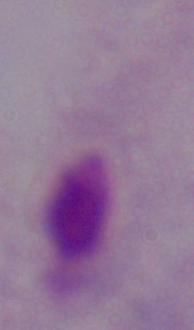

Summary:
  - Modality: micrograph
  - Magnification: 1000x
  - Identification: trichomonad